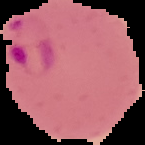
Summary:
  - Preparation: thin blood film
  - Image type: segmented cell region with the area outside set to black
  - Result: malaria parasites detected
  - Image size: 145×145 pixels